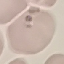

result = no malaria parasites detected
image type = cell patch, automatically extracted from a larger field of view and resized to 64 × 64 pixels
capture = smartphone through the microscope eyepiece
preparation = thin smear
stain = Giemsa